Locate every blood parasite and identify its species.
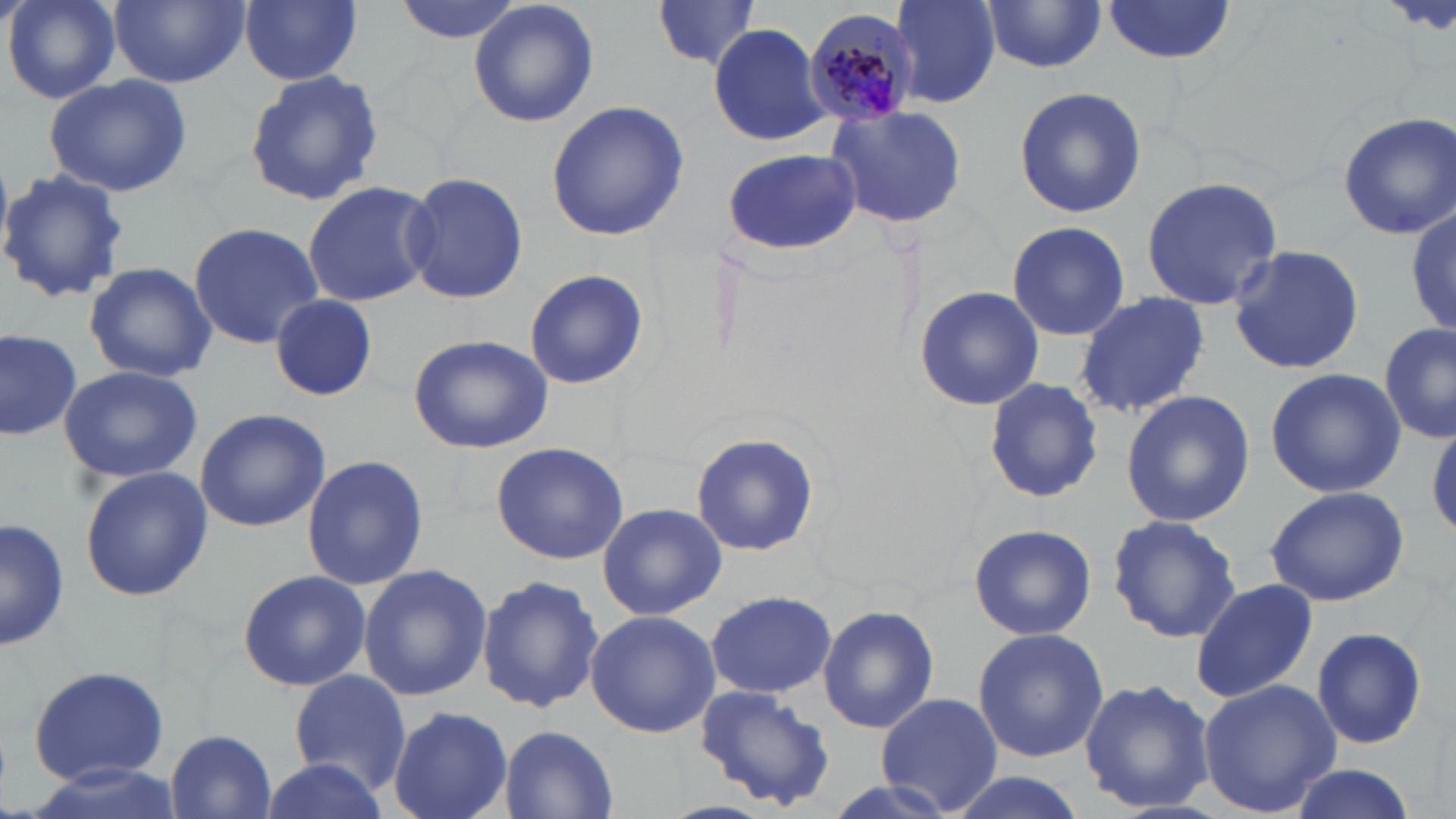
Approximate bounding boxes as [x1, y1, x2, y2] in pixels.
Plasmodium malariae-infected red blood cells: [803, 7, 919, 129].
No Plasmodium falciparum, Plasmodium ovale, Plasmodium vivax, Babesia divergens, or Trypanosoma brucei observed.

slide_level_diagnosis: Plasmodium malariae
modality: light microscopy
magnification: 1000x
uninfected_red_blood_cell_locations: 'approximate bounding boxes as [x1, y1, x2, y2] in pixels: [5, 0, 121, 104], [110, 0, 249, 91], [239, 0, 362, 87], [392, 0, 525, 44], [468, 0, 599, 128], [650, 1, 765, 71], [889, 1, 1000, 109], [1102, 1, 1238, 64], [981, 2, 1107, 75], [707, 23, 831, 145], [243, 68, 386, 208], [43, 73, 192, 197], [1015, 86, 1146, 219], [546, 99, 689, 241], [822, 101, 969, 231], [1336, 111, 1456, 239], [724, 148, 861, 256], [0, 167, 128, 306], [401, 169, 528, 306], [1139, 177, 1284, 311], [300, 180, 437, 308], [1407, 199, 1456, 344], [1003, 220, 1131, 341], [188, 222, 324, 349], [1227, 242, 1364, 378], [83, 261, 217, 384], [523, 269, 651, 389], [914, 287, 1046, 409], [1074, 291, 1209, 419], [271, 295, 377, 403], [1379, 322, 1456, 443], [0, 327, 81, 443], [408, 334, 554, 456], [59, 364, 202, 484], [1264, 368, 1407, 499], [982, 376, 1103, 505], [1121, 389, 1255, 528], [194, 408, 331, 533], [1429, 419, 1456, 540], [690, 430, 821, 556], [489, 441, 629, 566], [299, 454, 430, 591], [79, 463, 212, 602], [1264, 484, 1411, 607], [596, 503, 728, 620], [0, 515, 69, 653], [1106, 515, 1241, 643], [968, 523, 1095, 641], [358, 564, 492, 702], [236, 568, 372, 691], [477, 575, 604, 712], [1191, 578, 1321, 704], [705, 589, 837, 699], [817, 603, 939, 733], [584, 609, 720, 739], [1312, 626, 1429, 752], [972, 627, 1109, 762], [29, 664, 170, 787], [288, 668, 410, 794], [1078, 676, 1215, 815], [1197, 677, 1342, 817], [692, 684, 835, 812], [874, 692, 1003, 815], [386, 705, 513, 819], [496, 725, 619, 818], [167, 729, 277, 818], [253, 756, 391, 819], [1285, 765, 1421, 819], [941, 772, 1088, 819]'
stain: May-Grünwald-Giemsa
field_of_view: single
preparation: thin blood smear
image_size: 1456×819 pixels